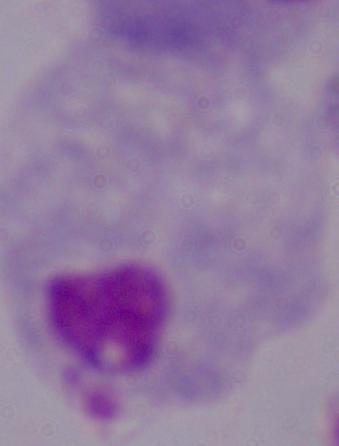
A trichomonad is seen. Micrograph. 1000x magnification.